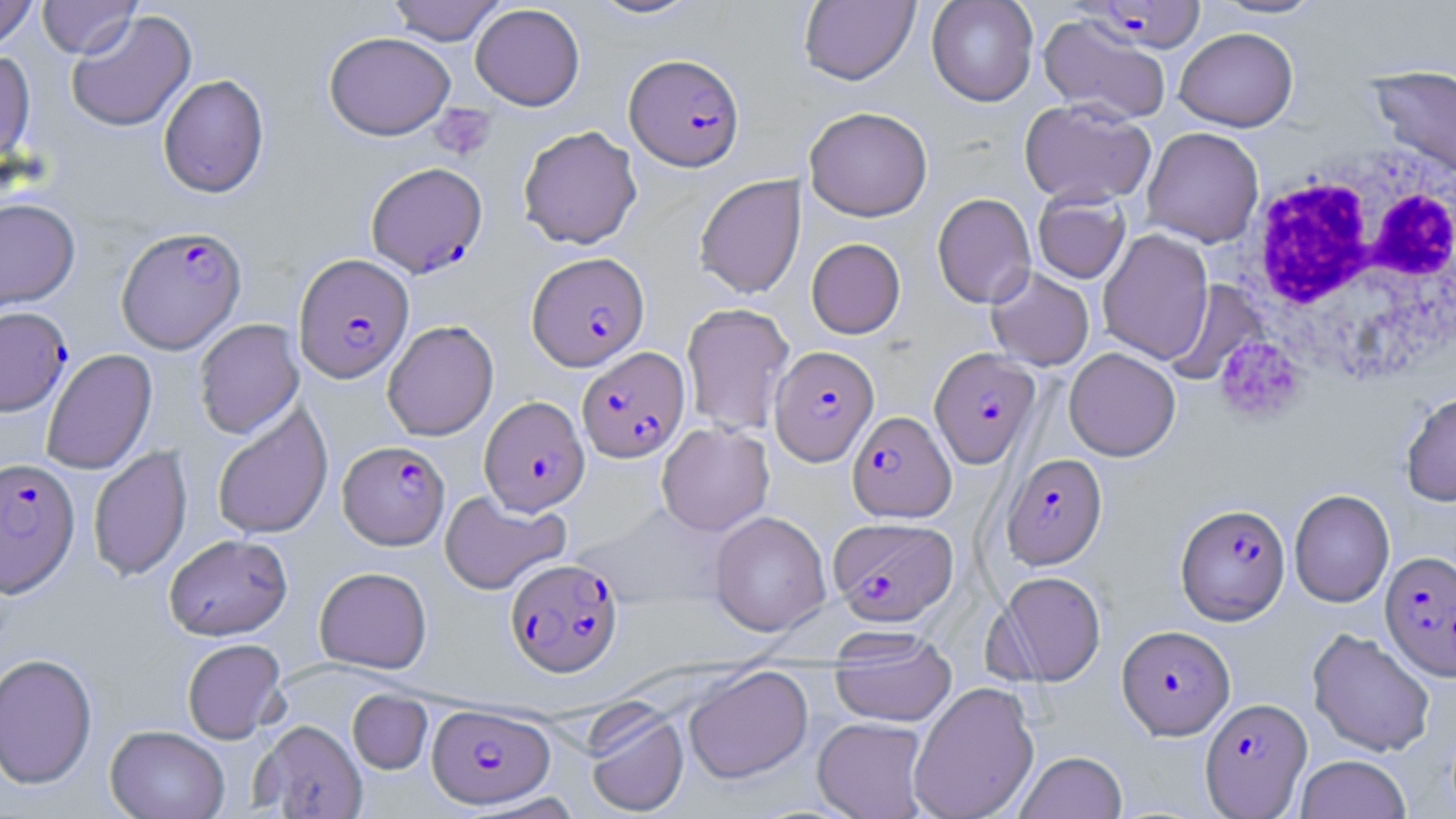

slide-level diagnosis = Plasmodium falciparum
magnification = 1000x
white blood cell locations = approximate bounding boxes as (x1, y1, x2, y2) in pixels: (1235, 144, 1456, 386)
stain = May-Grünwald-Giemsa
uninfected red blood cell locations = approximate bounding boxes as (x1, y1, x2, y2) in pixels: (0, 0, 38, 52), (38, 0, 141, 58), (387, 0, 507, 45), (586, 0, 704, 20), (799, 0, 919, 85), (926, 0, 1038, 106), (1207, 0, 1328, 20), (470, 4, 585, 110), (66, 10, 197, 133), (1038, 13, 1172, 124), (1175, 27, 1298, 132), (324, 31, 455, 140), (0, 49, 35, 166), (1368, 63, 1456, 180), (158, 74, 269, 198), (1019, 98, 1156, 207), (804, 106, 933, 221), (517, 125, 642, 249), (1142, 127, 1264, 247), (695, 174, 806, 299), (1033, 190, 1131, 284), (932, 192, 1036, 309), (0, 198, 80, 311), (1098, 229, 1213, 364), (806, 238, 905, 339), (986, 266, 1094, 371), (1165, 280, 1270, 387), (681, 302, 795, 436), (194, 318, 304, 440), (382, 320, 499, 441), (1064, 347, 1180, 461), (41, 348, 157, 475), (1401, 391, 1456, 506), (211, 403, 333, 540), (657, 423, 774, 536), (88, 445, 192, 581), (1289, 489, 1394, 607), (439, 490, 571, 595), (709, 511, 831, 636), (164, 533, 292, 640), (314, 567, 432, 673), (995, 571, 1106, 686), (1307, 627, 1436, 757), (830, 633, 957, 727), (182, 638, 286, 743), (0, 653, 98, 789), (683, 666, 813, 783), (908, 681, 1039, 819), (347, 690, 432, 774), (583, 704, 689, 817), (812, 717, 930, 819), (252, 719, 367, 818), (105, 725, 230, 818), (1015, 751, 1128, 819), (1295, 755, 1411, 819)
platelet locations = approximate bounding boxes as (x1, y1, x2, y2) in pixels: (431, 104, 497, 162), (1215, 337, 1306, 425)
field of view = one of a larger specimen
Plasmodium falciparum-infected red blood cell locations = approximate bounding boxes as (x1, y1, x2, y2) in pixels: (1080, 1, 1204, 53), (625, 53, 744, 171), (366, 161, 488, 278), (116, 226, 246, 353), (526, 252, 649, 371), (293, 253, 414, 383), (0, 306, 72, 416), (769, 345, 878, 465), (577, 346, 690, 464), (929, 348, 1041, 468), (480, 396, 590, 515), (847, 410, 955, 522), (338, 441, 450, 550), (1002, 453, 1106, 569), (0, 457, 80, 598), (1175, 503, 1290, 624), (828, 517, 958, 626), (1380, 550, 1456, 681), (506, 558, 622, 677), (1117, 625, 1234, 739), (1200, 697, 1312, 816), (427, 704, 555, 808)
modality = light microscopy
image size = 1456×819 pixels
preparation = thin blood film